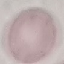

Summary:
  - Result: negative for malaria parasites
  - Capture: smartphone through the microscope eyepiece
  - Preparation: thin blood film
  - Image type: cell patch, automatically extracted from a larger field of view and resized to 64 × 64 pixels
  - Stain: Giemsa